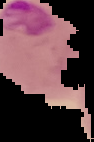

Image is 94×142 pixels. From a thin blood smear. Segmented cell region on a black background. Malaria status: parasitized.